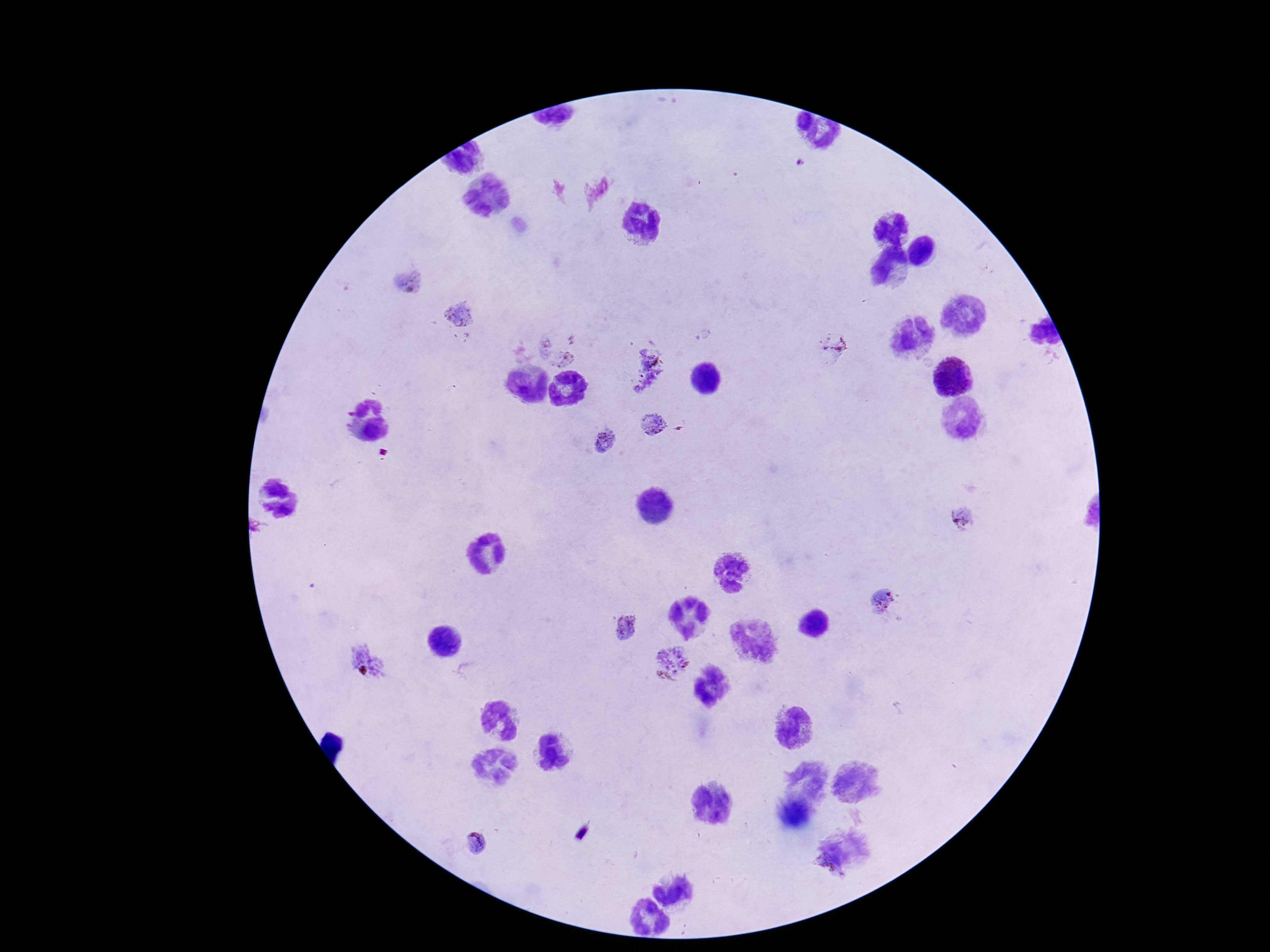 Approximate object centers, in pixels from the top-left corner. Plasmodium parasite locations: (x=406, y=281), (x=461, y=316), (x=563, y=343), (x=641, y=367), (x=653, y=426), (x=604, y=443), (x=964, y=517), (x=884, y=599), (x=625, y=626), (x=368, y=662), (x=672, y=663), (x=476, y=844). Patient malaria status: infected. Giemsa-stained preparation. 100x magnification. Photographed through the microscope eyepiece with a smartphone camera. Thick blood smear. Image is 1270×952 pixels. Single field of view.